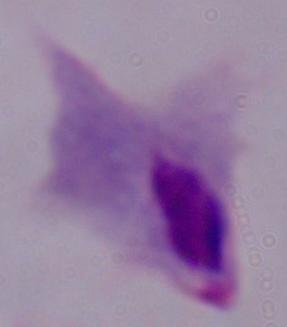
identification = trichomonad
modality = photomicrograph
magnification = 1000x